Report the malaria status of this cell.
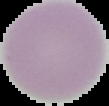
It is uninfected.

From a thin blood smear. Segmented cell region on a black background. Image is 109×106 pixels.